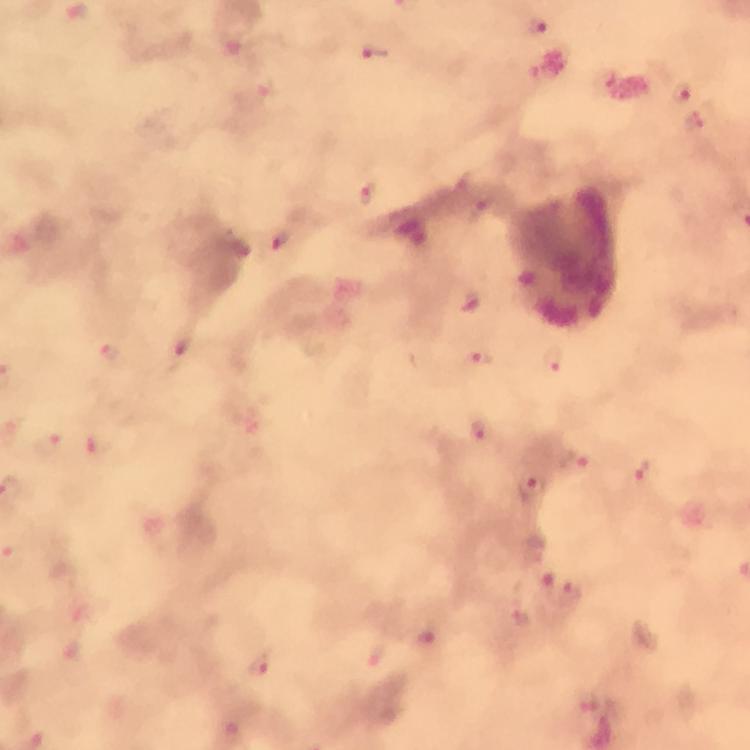
stain: Giemsa
capture: smartphone camera through the microscope
magnification: 100x
malaria_parasite_locations: 'approximate centers as [x, y] in pixels: [77, 13], [537, 28], [374, 53], [681, 93], [695, 124], [369, 194], [278, 241], [472, 303], [111, 353], [179, 354], [551, 361], [477, 363], [479, 430], [50, 445], [575, 465], [641, 473], [533, 489], [571, 592], [521, 617], [430, 640], [379, 657], [260, 667]'
preparation: thick smear
context: from a malaria diagnostic workup
cropped_from: a single field of view
immersion_oil: applied
image_size: 750×750 pixels